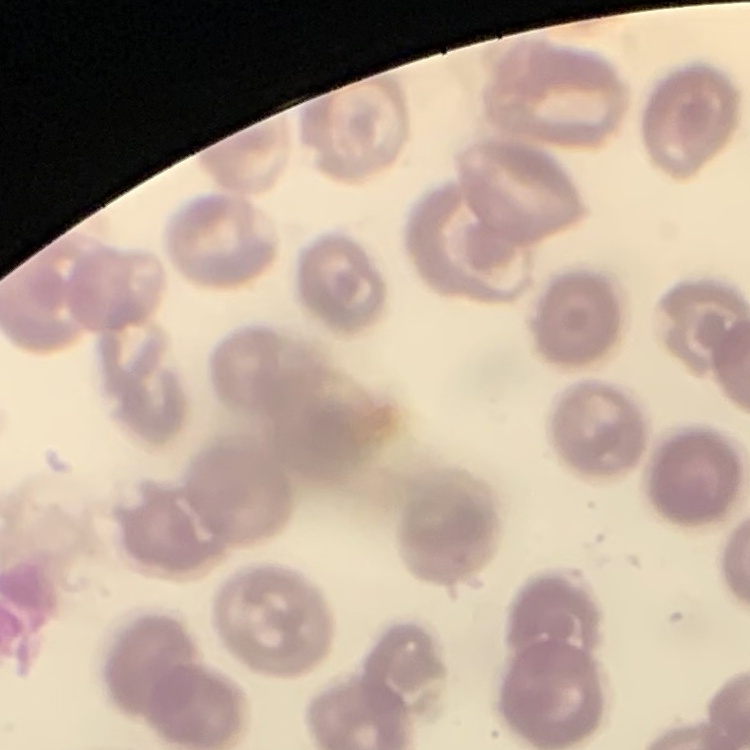
Summary:
  - Red blood cell morphology: no rouleaux formation
  - Image type: one tile cut from a larger photomicrograph
  - Stain: Field's or Giemsa
  - Preparation: thin blood film